Classify this cell by malaria status.
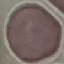
It is uninfected.

preparation = thin smear
capture = smartphone camera at the microscope eyepiece
image type = automatically extracted cell patch, resized to 64 × 64 pixels
stain = Giemsa